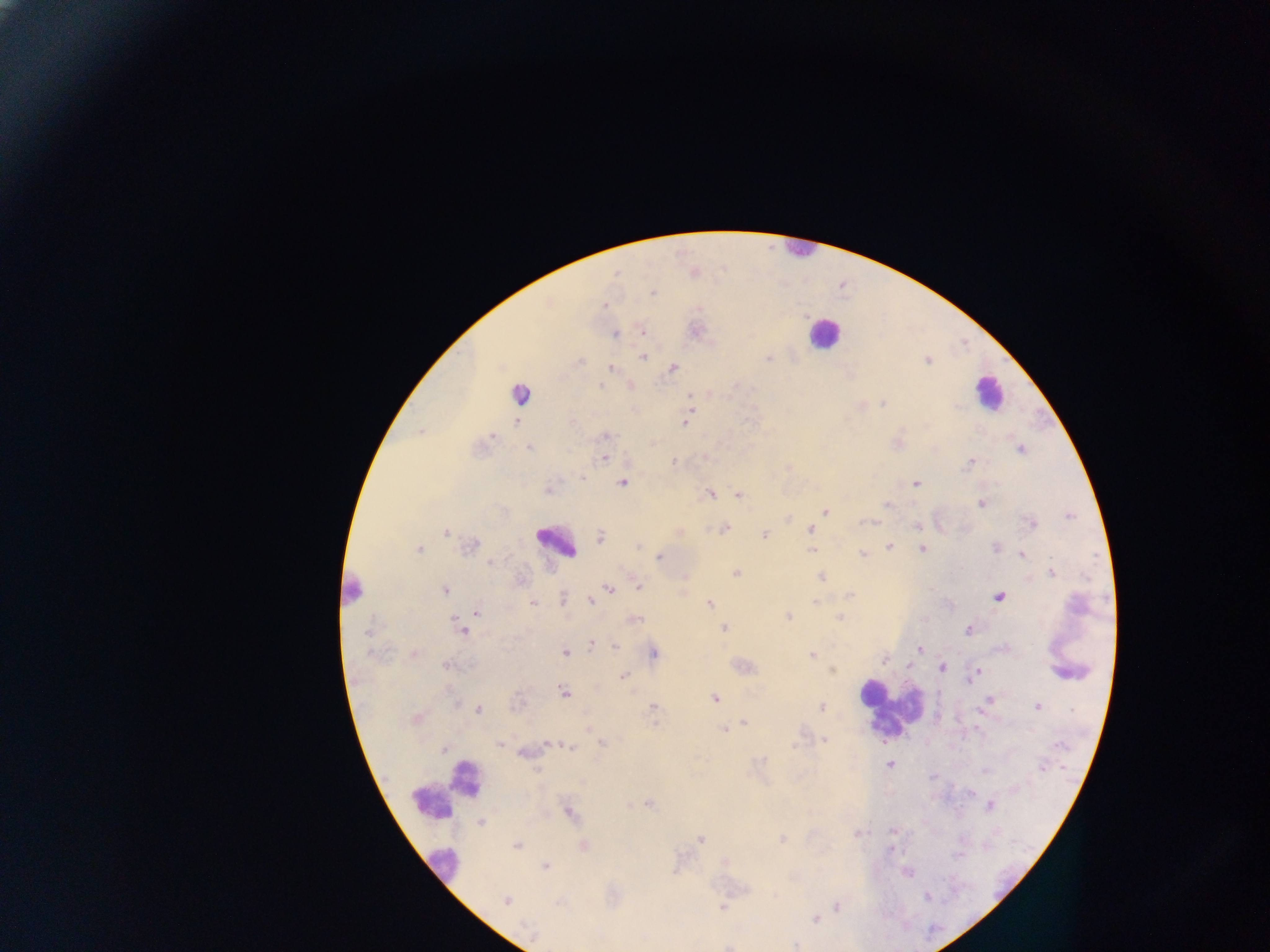
Approximate centers as (x, y) in pixels. Leukocyte locations: (798, 251), (823, 333), (989, 391), (520, 392), (555, 544), (351, 591), (889, 708), (445, 791), (444, 866). Plasmodium parasite locations: (616, 273), (653, 292), (605, 306), (643, 332), (615, 334), (642, 357), (768, 358), (927, 360), (611, 368), (673, 368), (600, 385), (690, 395), (883, 404), (516, 422), (685, 422), (421, 431), (492, 436), (606, 436), (529, 447), (1020, 449), (604, 458), (673, 462), (969, 463), (578, 475), (622, 482), (916, 483), (710, 494), (738, 494), (980, 503), (886, 505), (825, 511), (1070, 516), (870, 522), (917, 525), (1033, 525), (725, 529), (810, 529), (446, 532), (764, 535), (601, 537), (472, 544), (638, 546), (890, 546), (922, 548), (996, 548), (418, 549), (811, 551), (863, 554), (1022, 555), (659, 557), (491, 562), (735, 573), (1051, 573), (822, 577), (638, 587), (607, 589), (445, 590), (850, 595), (999, 597), (563, 598), (591, 601), (814, 602), (533, 603), (709, 603), (476, 611), (788, 618), (840, 618), (637, 619), (724, 628), (968, 630), (463, 631), (366, 633), (591, 644), (616, 646), (919, 649), (565, 652), (655, 653), (812, 654), (884, 660), (908, 665), (446, 666), (941, 668), (833, 671), (977, 672), (622, 676), (563, 691), (715, 699), (988, 699), (653, 706), (1037, 706), (821, 708), (479, 709), (416, 719), (744, 722), (724, 730), (824, 740), (601, 742), (500, 744), (549, 744), (796, 745), (1058, 745), (571, 747), (443, 749), (890, 764), (1042, 768), (537, 770), (649, 804), (990, 806), (571, 814), (481, 823), (893, 831), (858, 833), (701, 839), (781, 839), (516, 846), (584, 846), (545, 865), (907, 873), (927, 897), (505, 900), (558, 904), (837, 906), (722, 907), (816, 919), (796, 945). Collected in Ghana. Thick blood smear. Photographed through a microscope with a mobile-phone camera. Single field of view. Image is 1270×952 pixels.